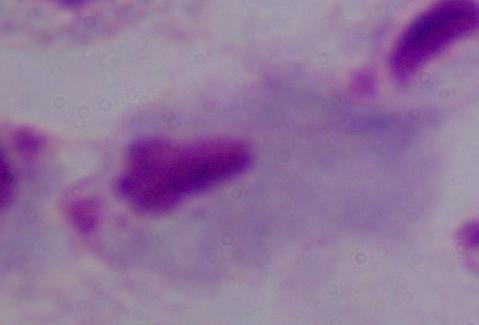
Summary:
  - Identification: trichomonad
  - Modality: photomicrograph
  - Magnification: 1000x